Assess this cell for malaria.
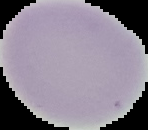

Uninfected.

image type = cell region segmented out of the field of view; surrounding area masked to black
preparation = thin blood film
image size = 148×130 pixels